State which parasite is depicted.
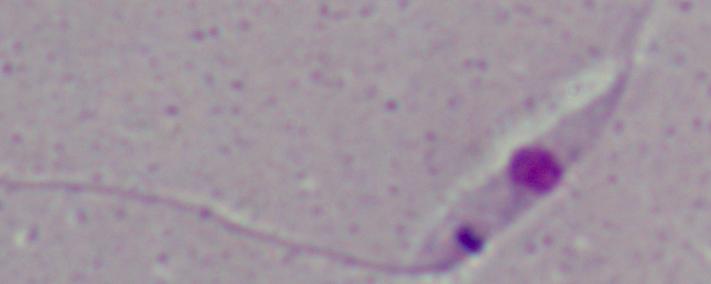

Leishmania.

Summary:
  - Modality: micrograph
  - Magnification: 1000x